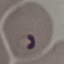
Result: malaria parasites detected. Automatically extracted cell patch, resized to 64 × 64 pixels. Thin smear of blood. Giemsa stain. Photographed with a smartphone camera at the microscope eyepiece.